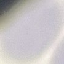

Summary:
  - Malaria status: uninfected
  - Stain: Giemsa
  - Capture: smartphone camera at the microscope eyepiece
  - Preparation: thin smear
  - Image type: cell patch, automatically extracted from a larger field of view and resized to 64 × 64 pixels